State which parasite is depicted.
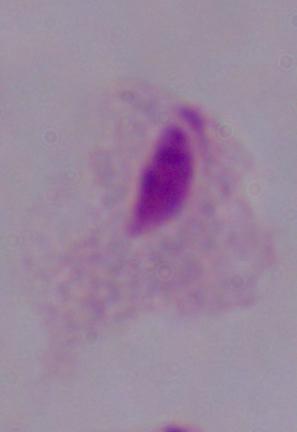
A trichomonad.

Summary:
  - Magnification: 1000x
  - Modality: micrograph